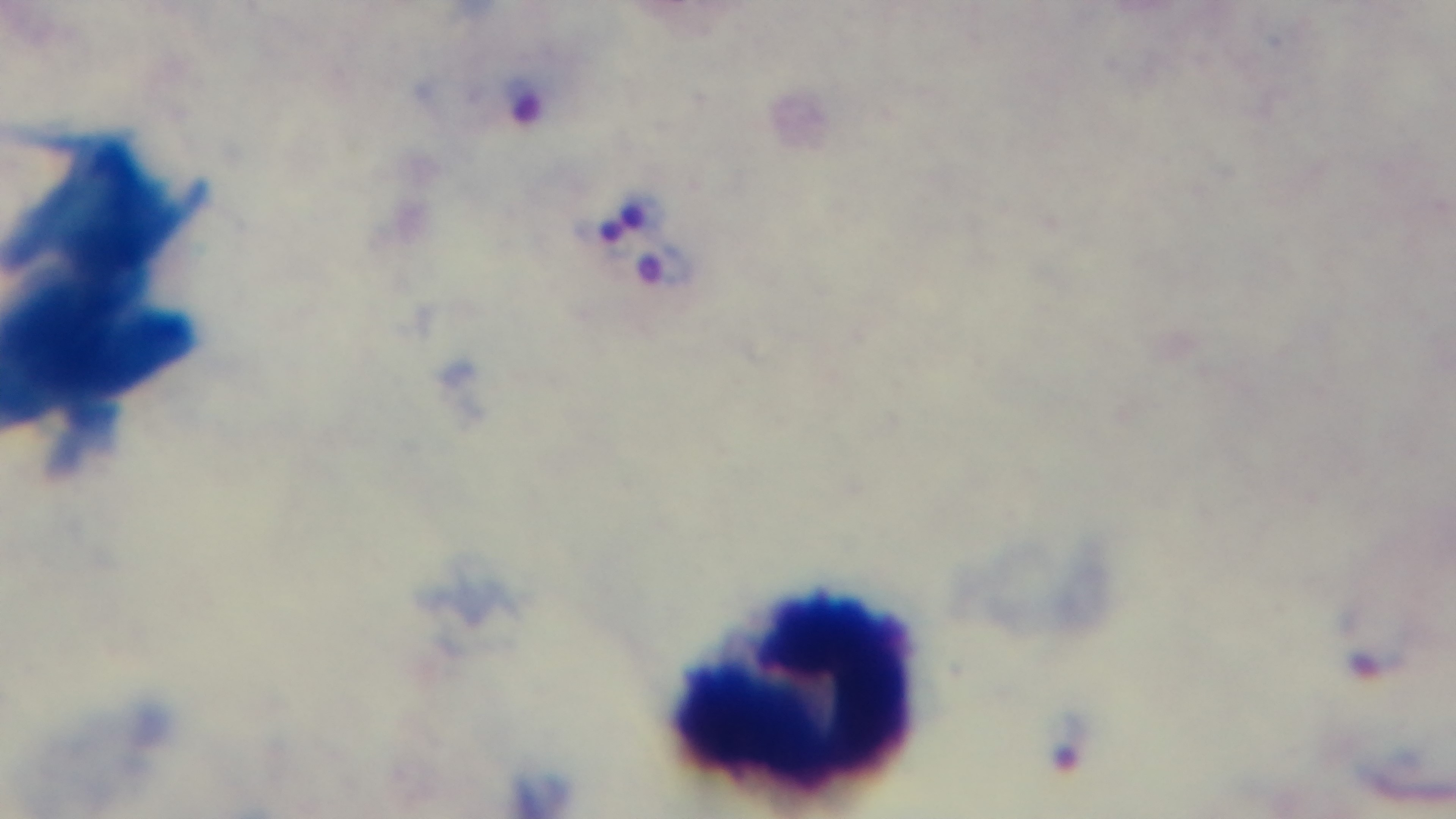 Malaria status: infected. Captured with a mounted 4K digital camera. Light microscopy. Giemsa stain. Preparation: thick blood film. Single field of view. Oil-immersion objective, 100x.